Report the malaria status of this cell.
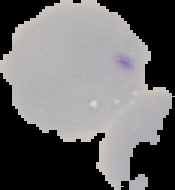
Uninfected.

The area outside the segmented cell region is set to black. From a thin blood smear. Image is 175×190 pixels.